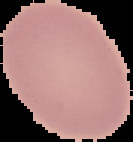
malaria_status: uninfected
preparation: thin blood smear
image_size: 133×142 pixels
image_type: segmented cell region on a black background